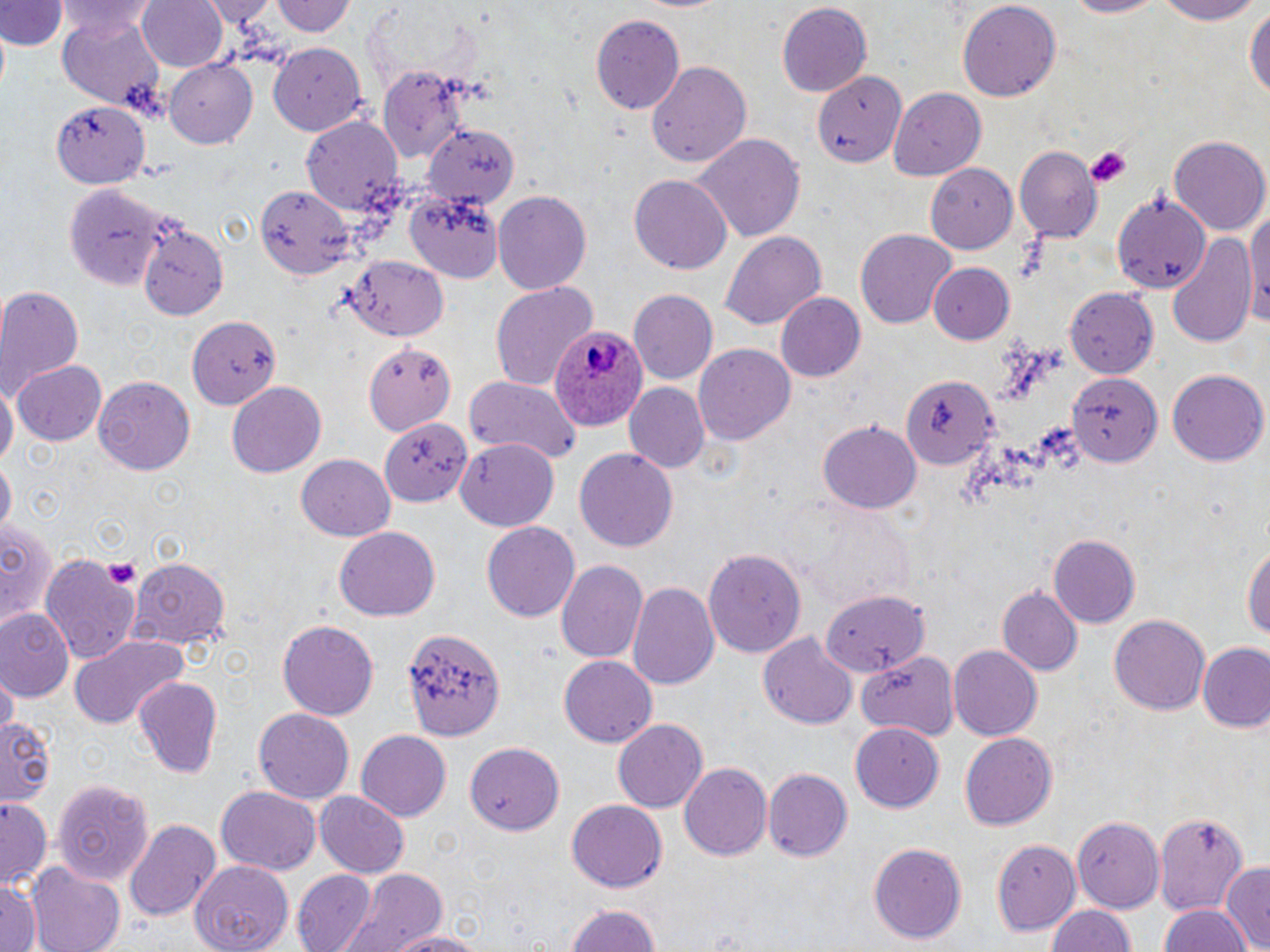
slide_level_diagnosis: Plasmodium ovale
field_of_view: single
stain: May-Grünwald-Giemsa
uninfected_red_blood_cell_locations: 'approximate bounding boxes as named x1/y1/x2/y2 corners in pixels: (x1=137, y1=0, x2=228, y2=72), (x1=201, y1=0, x2=280, y2=26), (x1=275, y1=0, x2=353, y2=39), (x1=636, y1=0, x2=735, y2=15), (x1=957, y1=0, x2=1061, y2=100), (x1=1054, y1=0, x2=1164, y2=19), (x1=1150, y1=0, x2=1263, y2=26), (x1=0, y1=1, x2=64, y2=52), (x1=58, y1=2, x2=162, y2=43), (x1=1244, y1=2, x2=1270, y2=108), (x1=774, y1=3, x2=874, y2=98), (x1=57, y1=14, x2=166, y2=110), (x1=591, y1=14, x2=685, y2=114), (x1=268, y1=43, x2=369, y2=135), (x1=166, y1=59, x2=258, y2=147), (x1=645, y1=59, x2=752, y2=171), (x1=373, y1=64, x2=468, y2=160), (x1=809, y1=66, x2=903, y2=172), (x1=891, y1=87, x2=987, y2=178), (x1=54, y1=103, x2=146, y2=190), (x1=301, y1=114, x2=403, y2=215), (x1=422, y1=125, x2=519, y2=211), (x1=695, y1=134, x2=805, y2=243), (x1=1169, y1=135, x2=1269, y2=237), (x1=1014, y1=147, x2=1102, y2=241), (x1=927, y1=166, x2=1018, y2=254), (x1=630, y1=174, x2=732, y2=275), (x1=65, y1=181, x2=170, y2=287), (x1=256, y1=183, x2=354, y2=276), (x1=492, y1=190, x2=592, y2=295), (x1=404, y1=192, x2=501, y2=280), (x1=1114, y1=192, x2=1211, y2=294), (x1=1246, y1=201, x2=1270, y2=329), (x1=134, y1=209, x2=233, y2=322), (x1=856, y1=228, x2=957, y2=330), (x1=720, y1=230, x2=826, y2=334), (x1=1169, y1=231, x2=1259, y2=349), (x1=875, y1=245, x2=1010, y2=335), (x1=342, y1=256, x2=448, y2=342), (x1=929, y1=264, x2=1016, y2=344), (x1=489, y1=282, x2=596, y2=390), (x1=0, y1=285, x2=83, y2=393), (x1=1064, y1=285, x2=1159, y2=379), (x1=775, y1=290, x2=865, y2=381), (x1=628, y1=291, x2=718, y2=384), (x1=185, y1=312, x2=279, y2=411), (x1=364, y1=341, x2=455, y2=434), (x1=694, y1=344, x2=794, y2=443), (x1=11, y1=360, x2=108, y2=445), (x1=1069, y1=369, x2=1163, y2=467), (x1=1169, y1=369, x2=1266, y2=467), (x1=900, y1=373, x2=996, y2=468), (x1=465, y1=374, x2=583, y2=463), (x1=94, y1=378, x2=195, y2=472), (x1=1, y1=379, x2=16, y2=474), (x1=228, y1=381, x2=326, y2=476), (x1=624, y1=381, x2=709, y2=472), (x1=378, y1=416, x2=470, y2=506), (x1=819, y1=419, x2=921, y2=514), (x1=456, y1=440, x2=559, y2=530), (x1=576, y1=448, x2=678, y2=554), (x1=297, y1=454, x2=394, y2=540), (x1=1, y1=459, x2=14, y2=537), (x1=800, y1=503, x2=916, y2=607), (x1=482, y1=519, x2=580, y2=619), (x1=0, y1=522, x2=59, y2=631), (x1=334, y1=525, x2=441, y2=622), (x1=1049, y1=534, x2=1140, y2=627), (x1=1244, y1=538, x2=1270, y2=648), (x1=703, y1=545, x2=805, y2=656), (x1=40, y1=552, x2=142, y2=665), (x1=131, y1=555, x2=231, y2=647), (x1=556, y1=559, x2=649, y2=665), (x1=628, y1=580, x2=720, y2=690), (x1=996, y1=587, x2=1082, y2=675), (x1=818, y1=588, x2=930, y2=674), (x1=819, y1=589, x2=933, y2=675), (x1=0, y1=608, x2=73, y2=700), (x1=1109, y1=614, x2=1212, y2=715), (x1=278, y1=621, x2=377, y2=721), (x1=400, y1=627, x2=504, y2=739), (x1=69, y1=634, x2=190, y2=731), (x1=758, y1=635, x2=855, y2=728), (x1=947, y1=645, x2=1039, y2=741), (x1=1199, y1=646, x2=1269, y2=732), (x1=857, y1=653, x2=960, y2=740), (x1=558, y1=654, x2=659, y2=746), (x1=3, y1=672, x2=16, y2=740), (x1=133, y1=677, x2=222, y2=778), (x1=253, y1=708, x2=356, y2=803), (x1=2, y1=715, x2=55, y2=806), (x1=613, y1=717, x2=707, y2=813), (x1=851, y1=723, x2=945, y2=811), (x1=356, y1=730, x2=451, y2=822), (x1=960, y1=731, x2=1058, y2=831), (x1=465, y1=740, x2=563, y2=835), (x1=680, y1=760, x2=772, y2=862), (x1=764, y1=768, x2=850, y2=863), (x1=52, y1=776, x2=156, y2=888), (x1=216, y1=787, x2=320, y2=875), (x1=315, y1=791, x2=407, y2=877), (x1=0, y1=798, x2=52, y2=891), (x1=567, y1=798, x2=667, y2=892), (x1=1153, y1=810, x2=1251, y2=921), (x1=1073, y1=816, x2=1164, y2=913), (x1=124, y1=819, x2=219, y2=918), (x1=993, y1=837, x2=1081, y2=933), (x1=868, y1=842, x2=967, y2=944), (x1=191, y1=861, x2=296, y2=952), (x1=1221, y1=862, x2=1270, y2=950), (x1=28, y1=863, x2=126, y2=952), (x1=293, y1=869, x2=376, y2=952), (x1=343, y1=870, x2=452, y2=952), (x1=0, y1=880, x2=41, y2=952), (x1=562, y1=902, x2=666, y2=952), (x1=1044, y1=905, x2=1136, y2=952), (x1=1155, y1=905, x2=1250, y2=952), (x1=383, y1=930, x2=488, y2=952)'
modality: optical microscopy
image_size: 1270×952 pixels
preparation: thin blood film
platelet_locations: 'approximate bounding boxes as named x1/y1/x2/y2 corners in pixels: (x1=1085, y1=147, x2=1132, y2=188), (x1=104, y1=556, x2=141, y2=591)'
plasmodium_ovale_infected_red_blood_cell_locations: 'approximate bounding boxes as named x1/y1/x2/y2 corners in pixels: (x1=548, y1=325, x2=647, y2=433)'
magnification: 1000x